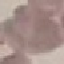 Malaria status: uninfected. Acquired by smartphone through the microscope eyepiece. Thin smear of blood. Automatically extracted cell patch, resized to 64 × 64 pixels. Giemsa stain.